Report the malaria status of this cell.
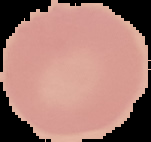

Uninfected.

Image is 151×142 pixels. From a thin blood film. Cell region segmented out of the field of view; the surrounding area is masked to black.